Outline each blood parasite and name the species.
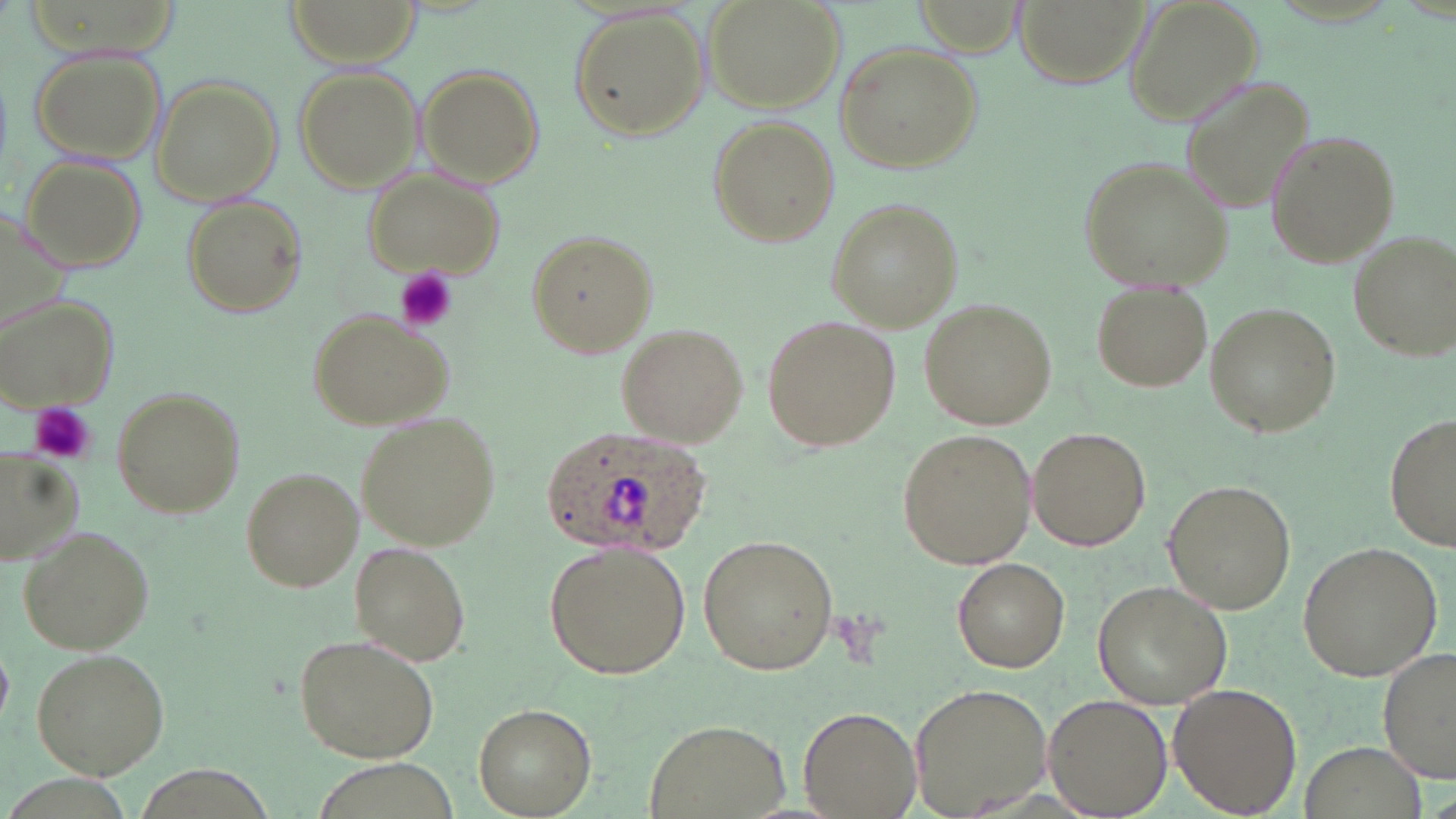

Approximate bounding boxes as [x1, y1, x2, y2] in pixels.
Plasmodium ovale-infected red blood cells: [540, 425, 709, 560].
No Plasmodium falciparum, Plasmodium malariae, Plasmodium vivax, Babesia divergens, or Trypanosoma brucei observed.

Summary:
  - Uninfected red blood cell locations: [287, 0, 419, 65], [706, 0, 845, 114], [1007, 0, 1158, 93], [1125, 0, 1264, 121], [569, 5, 709, 141], [833, 42, 983, 175], [26, 44, 168, 167], [292, 65, 423, 192], [417, 65, 545, 187], [150, 76, 283, 205], [1181, 78, 1318, 215], [710, 116, 839, 246], [1266, 128, 1398, 267], [22, 156, 149, 273], [1079, 156, 1234, 292], [360, 168, 504, 279], [182, 195, 306, 315], [826, 197, 966, 330], [526, 228, 658, 357], [1347, 229, 1455, 362], [1093, 281, 1214, 393], [0, 294, 122, 412], [918, 300, 1055, 429], [1205, 304, 1340, 437], [308, 312, 453, 429], [760, 313, 899, 453], [615, 323, 747, 445], [111, 387, 244, 519], [355, 412, 501, 551], [1384, 415, 1456, 553], [1028, 426, 1150, 549], [896, 428, 1035, 568], [2, 455, 79, 560], [241, 468, 363, 591], [1163, 479, 1295, 615], [17, 525, 155, 656], [697, 533, 840, 676], [543, 540, 692, 680], [1298, 540, 1443, 683], [349, 544, 469, 664], [953, 558, 1067, 673], [1091, 579, 1232, 708], [293, 633, 440, 764], [1378, 646, 1455, 781], [30, 648, 170, 778], [908, 680, 1056, 819], [1167, 682, 1302, 815], [1044, 694, 1172, 815], [474, 703, 594, 816], [799, 705, 921, 816], [644, 720, 791, 817]
  - Platelet locations: [395, 268, 458, 331], [30, 402, 95, 465]
  - Slide-level diagnosis: Plasmodium ovale
  - Modality: optical microscopy
  - Preparation: thin blood smear
  - Field of view: single
  - Image size: 1456×819 pixels
  - Magnification: 1000x
  - Stain: May-Grünwald-Giemsa